State which cell type is depicted.
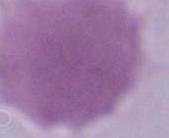
This is an erythrocyte.

modality = micrograph
magnification = 1000x